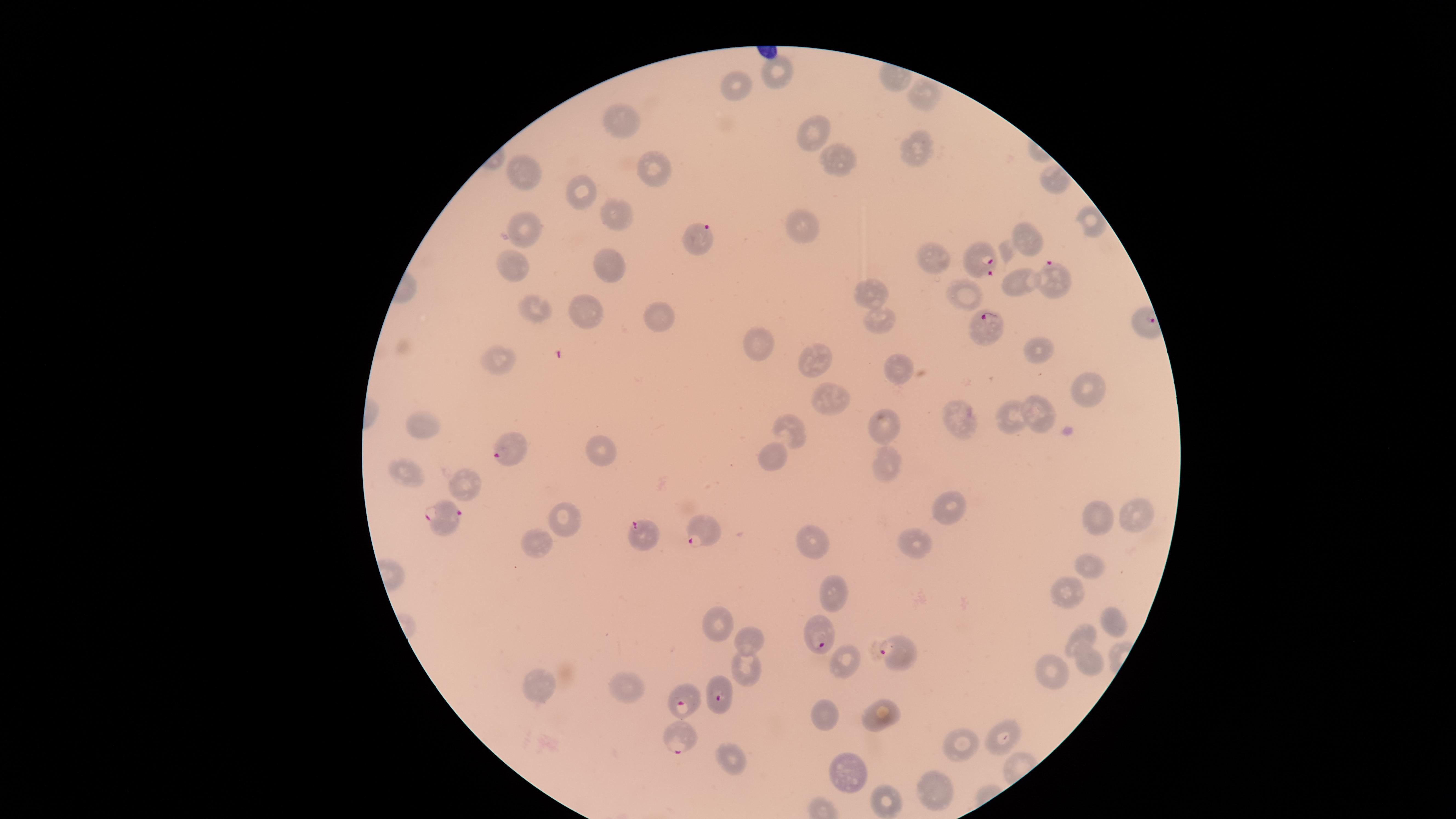
Approximate marker points as {x, y} in pixels.
Summary:
  - Parasitized red blood cells: {706, 242}, {981, 260}, {1055, 279}, {989, 328}, {510, 453}, {441, 516}, {706, 528}, {642, 533}, {820, 636}, {900, 654}, {717, 690}, {687, 696}, {684, 733}
  - Uninfected red blood cells: {777, 75}, {738, 84}, {918, 95}, {624, 119}, {816, 128}, {917, 152}, {835, 162}, {523, 168}, {653, 169}, {1055, 182}, {582, 188}, {616, 218}, {1090, 225}, {805, 230}, {524, 231}, {1027, 241}, {937, 259}, {610, 261}, {508, 262}, {1023, 285}, {869, 290}, {965, 296}, {535, 308}, {577, 311}, {659, 319}, {876, 320}, {756, 337}, {1034, 349}, {503, 362}, {820, 364}, {894, 368}, {1089, 392}, {827, 402}, {1041, 411}, {1007, 414}, {959, 423}, {422, 424}, {884, 424}, {786, 427}, {603, 450}, {772, 454}, {883, 463}, {405, 469}, {468, 484}, {950, 509}, {1139, 516}, {570, 517}, {1098, 519}, {920, 538}, {812, 542}, {537, 545}, {1093, 567}, {1066, 589}, {832, 590}, {716, 621}, {1107, 621}, {746, 634}, {1080, 640}, {1082, 658}, {845, 660}, {747, 668}, {1050, 674}, {634, 685}, {536, 686}, {829, 716}, {879, 716}, {1002, 731}, {956, 742}, {730, 756}, {848, 776}, {930, 785}, {885, 797}
  - Presence: malaria parasites detected
  - Image size: 1456×819 pixels
  - Field of view: single
  - Capture: smartphone photograph through the microscope eyepiece
  - Stain: Giemsa
  - Preparation: thin blood film
  - Visible region: circular
  - Species: Plasmodium falciparum